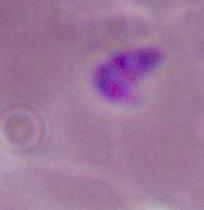

Summary:
  - Modality: micrograph
  - Magnification: 400x or 1000x
  - Identification: Plasmodium